Give the extent of all Babesia divergens-infected red blood cells.
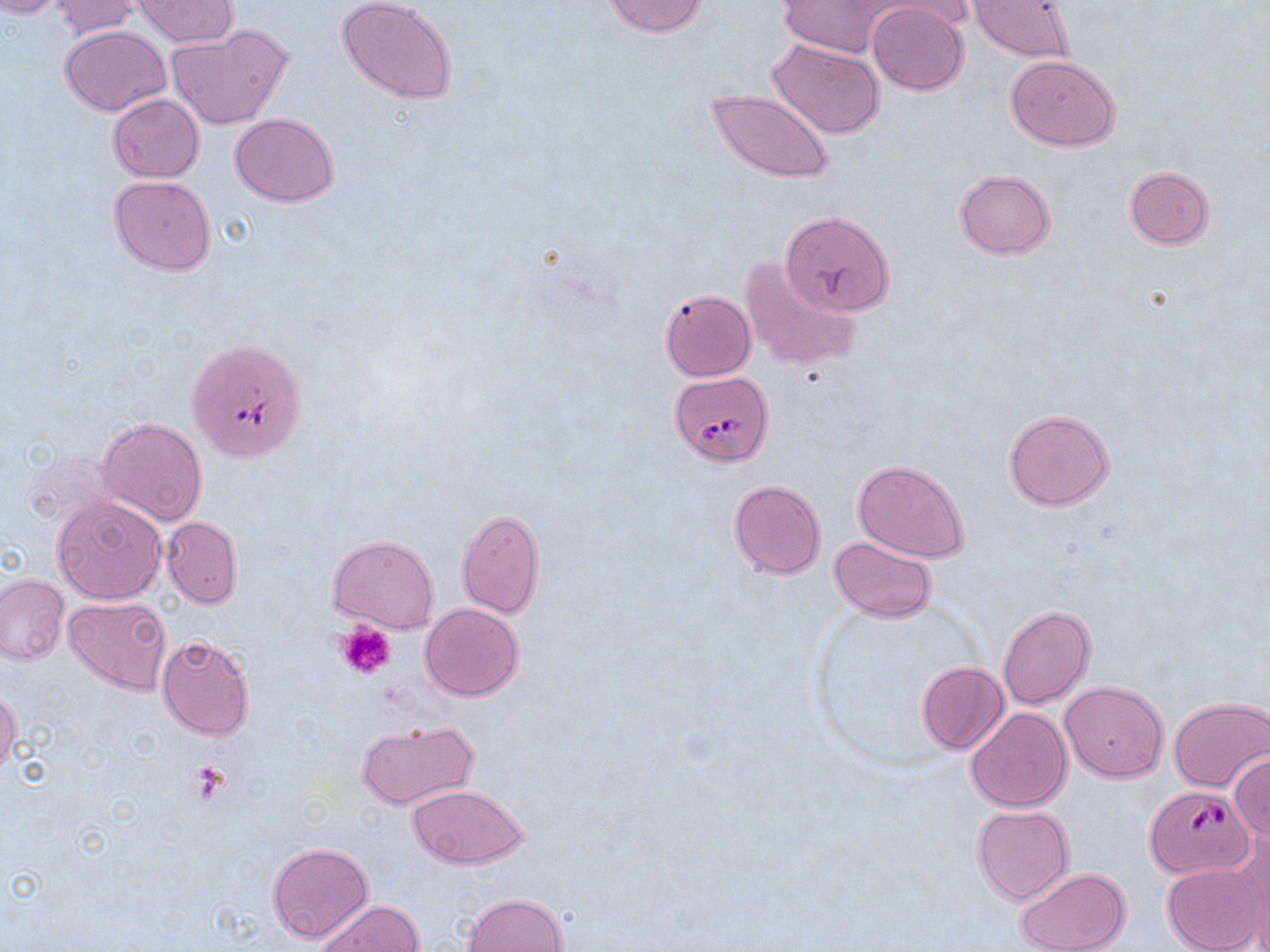
Approximate bounding boxes as (x1,y1)-(x2,y2) corner pairs in pixels.
Babesia divergens-infected red blood cells: (187,344)-(301,464), (670,370)-(774,465), (1144,785)-(1253,879).

Uninfected red blood cell locations: (0,0)-(74,17), (133,0)-(236,47), (337,0)-(458,105), (776,0)-(893,58), (868,0)-(978,36), (968,0)-(1077,62), (50,1)-(149,38), (602,1)-(709,37), (866,2)-(969,96), (166,24)-(294,131), (59,25)-(170,116), (768,39)-(886,139), (1006,54)-(1119,150), (705,89)-(834,184), (108,95)-(203,182), (230,113)-(339,205), (1124,166)-(1216,250), (953,169)-(1056,259), (109,174)-(216,274), (780,209)-(895,317), (740,257)-(861,372), (660,289)-(756,381), (1003,407)-(1114,511), (97,416)-(208,527), (852,458)-(969,564), (728,480)-(827,578), (51,493)-(167,604), (457,509)-(546,619), (161,515)-(242,608), (327,534)-(439,634), (829,536)-(938,623), (0,574)-(69,665), (64,595)-(172,694), (419,602)-(524,702), (998,604)-(1095,710), (156,635)-(258,741), (916,660)-(1009,756), (1059,680)-(1168,781), (0,688)-(21,776), (1169,697)-(1270,792), (965,706)-(1073,811), (355,720)-(480,810), (1230,752)-(1270,842), (405,785)-(529,869), (972,805)-(1076,904), (1230,829)-(1270,946), (266,841)-(374,943), (1162,863)-(1264,952), (1015,867)-(1130,952), (460,892)-(570,952), (319,900)-(424,952). Platelet locations: (337,621)-(397,681), (189,759)-(232,805). Slide-level diagnosis: Babesia divergens. Optical microscopy. May-Grünwald-Giemsa-stained preparation. Captured at 1000x magnification. Image is 1270×952 pixels. Thin blood smear. One field of a larger specimen.